Report the malaria status of this cell.
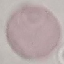

It is uninfected.

capture = smartphone through the microscope eyepiece
image type = automatically extracted cell patch, resized to 64 × 64 pixels
preparation = thin blood film
stain = Giemsa